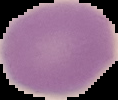
Summary:
  - Preparation: thin blood film
  - Malaria status: uninfected
  - Image size: 118×100 pixels
  - Image type: cell region segmented out of the field of view; surrounding area masked to black